Give the position of every Plasmodium parasite and every leukocyte.
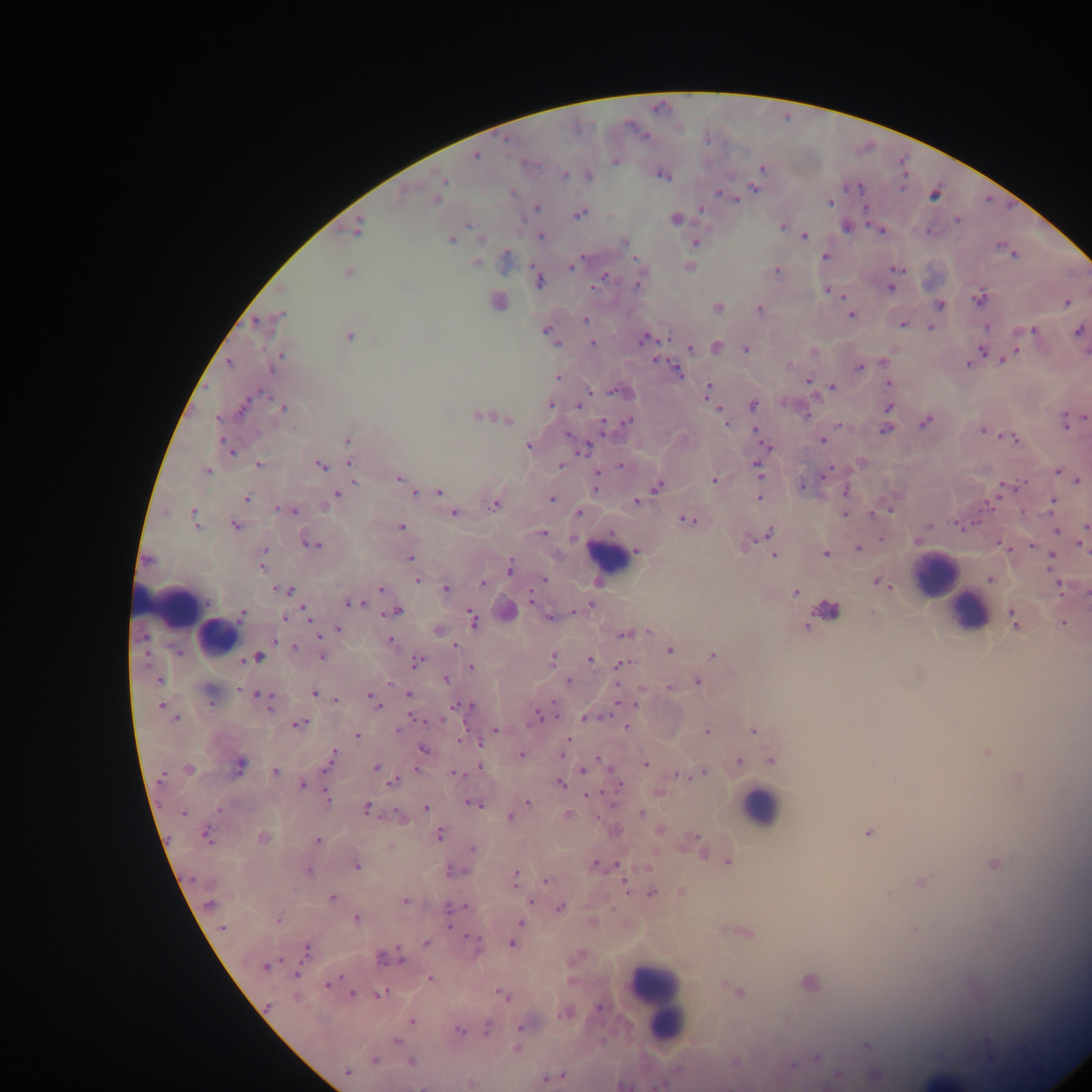

Approximate centers as [x, y] in pixels.
Plasmodium parasites: [475, 156], [615, 161], [761, 169], [565, 175], [662, 175], [589, 176], [443, 180], [755, 189], [512, 192], [935, 194], [726, 196], [436, 201], [830, 202], [536, 208], [702, 210], [579, 213], [675, 220], [958, 220], [782, 227], [846, 227], [357, 229], [880, 231], [540, 236], [805, 237], [450, 240], [624, 242], [696, 242], [506, 256], [825, 257], [476, 262], [573, 266], [689, 267], [898, 269], [777, 272], [348, 273], [602, 279], [538, 280], [638, 282], [596, 285], [890, 289], [828, 290], [980, 298], [498, 302], [1066, 303], [939, 305], [717, 307], [759, 309], [282, 315], [851, 315], [585, 320], [256, 322], [902, 324], [987, 327], [931, 328], [1032, 330], [546, 332], [1079, 332], [350, 336], [644, 339], [593, 344], [716, 346], [746, 348], [690, 349], [981, 351], [1005, 358], [277, 361], [229, 362], [884, 362], [969, 363], [790, 365], [859, 367], [675, 370], [557, 377], [809, 381], [889, 384], [832, 388], [708, 390], [618, 391], [551, 405], [580, 405], [753, 405], [243, 407], [888, 407], [284, 408], [806, 415], [477, 416], [722, 416], [1082, 418], [504, 420], [628, 420], [726, 422], [925, 423], [1068, 423], [604, 424], [886, 429], [983, 431], [757, 432], [569, 436], [1013, 438], [347, 441], [822, 441], [528, 446], [586, 447], [230, 451], [349, 461], [862, 462], [259, 465], [320, 465], [562, 465], [620, 466], [758, 469], [207, 471], [1058, 473], [399, 478], [595, 480], [714, 480], [1077, 481], [354, 482], [658, 486], [802, 487], [846, 491], [440, 492], [1000, 492], [414, 493], [337, 494], [759, 498], [247, 499], [552, 499], [636, 502], [1053, 502], [325, 505], [494, 506], [280, 509], [290, 511], [888, 511], [579, 513], [453, 514], [845, 514], [193, 516], [687, 520], [235, 525], [963, 525], [929, 526], [400, 527], [1086, 527], [1056, 530], [542, 532], [770, 533], [312, 543], [744, 544], [1003, 545], [1032, 546], [1083, 546], [858, 548], [264, 550], [636, 552], [825, 553], [774, 554], [264, 557], [1052, 557], [410, 559], [148, 560], [261, 566], [510, 567], [417, 580], [543, 580], [991, 580], [483, 582], [880, 583], [1059, 585], [381, 589], [446, 589], [286, 590], [795, 592], [1086, 593], [531, 598], [360, 602], [351, 603], [587, 607], [397, 612], [306, 613], [243, 614], [827, 614], [550, 617], [284, 618], [472, 620], [1013, 620], [310, 621], [1063, 623], [810, 625], [338, 629], [438, 631], [318, 634], [625, 635], [143, 637], [275, 641], [390, 641], [455, 646], [294, 647], [670, 650], [713, 655], [258, 657], [322, 657], [553, 657], [590, 660], [417, 662], [623, 664], [471, 668], [445, 679], [160, 681], [568, 681], [697, 682], [669, 688], [239, 690], [314, 693], [409, 694], [208, 695], [263, 695], [371, 699], [336, 700], [266, 701], [160, 705], [460, 705], [270, 707], [538, 716], [587, 718], [176, 719], [415, 719], [300, 724], [627, 727], [398, 730], [495, 730], [753, 730], [707, 732], [357, 735], [461, 738], [567, 740], [424, 750], [563, 752], [988, 752], [333, 754], [522, 755], [739, 761], [771, 761], [328, 764], [645, 764], [240, 765], [376, 767], [480, 767], [188, 769], [584, 770], [275, 771], [381, 771], [457, 773], [701, 773], [162, 774], [393, 783], [560, 784], [618, 784], [303, 785], [588, 795], [327, 798], [527, 802], [473, 804], [426, 807], [367, 808], [219, 810], [183, 813], [641, 813], [568, 816], [400, 817], [510, 818], [659, 831], [868, 833], [206, 835], [439, 835], [263, 838], [318, 841], [698, 844], [472, 848], [728, 861], [994, 864], [596, 865], [357, 866], [451, 871], [308, 872], [516, 876], [547, 880], [920, 882], [625, 884], [652, 894], [331, 898], [405, 901], [530, 901], [209, 905], [465, 907], [560, 908], [448, 909], [278, 920], [356, 920], [520, 922], [222, 928], [748, 933], [470, 937], [426, 943], [513, 944], [306, 950], [388, 957], [399, 957], [265, 967], [295, 975], [429, 979], [809, 982], [329, 984], [738, 992], [352, 994], [380, 994], [502, 994], [598, 1008], [565, 1014], [411, 1021], [488, 1028], [521, 1029], [460, 1031], [397, 1042], [866, 1046], [517, 1049], [817, 1058], [374, 1060], [410, 1062], [792, 1066], [347, 1072], [837, 1075], [876, 1077], [553, 1078], [470, 1084], [655, 1086].
Leukocytes: [602, 553], [935, 576], [161, 602], [967, 611], [218, 636], [761, 807], [655, 999].

country = Ghana
capture = mobile-phone photograph through a microscope
preparation = thick blood film
image size = 1092×1092 pixels
field of view = single